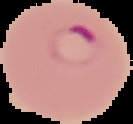
malaria status = parasitized
image size = 133×124 pixels
image type = cell region segmented out of the field of view; surrounding area masked to black
preparation = thin blood film